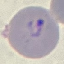

Result: malaria parasites detected. Giemsa stain. Thin blood smear. Acquired by smartphone through the microscope eyepiece. Automatically extracted cell patch, resized to 64 × 64 pixels.